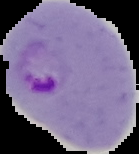
Segmented cell region on a black background. Result: Plasmodium parasites detected. Image is 139×154 pixels. From a thin blood smear.